Identify the parasite.
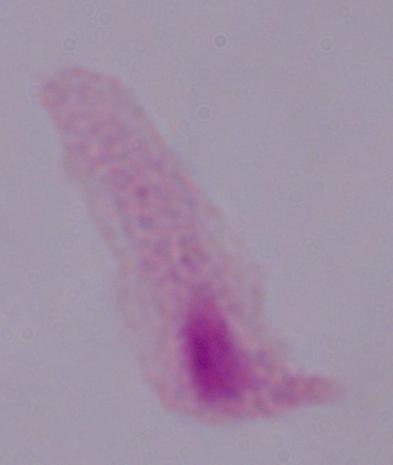

A trichomonad.

1000x magnification. Photomicrograph.